State which parasite is depicted.
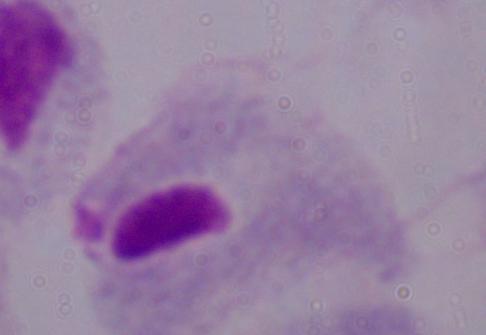

This is a trichomonad.

magnification = 1000x
modality = photomicrograph